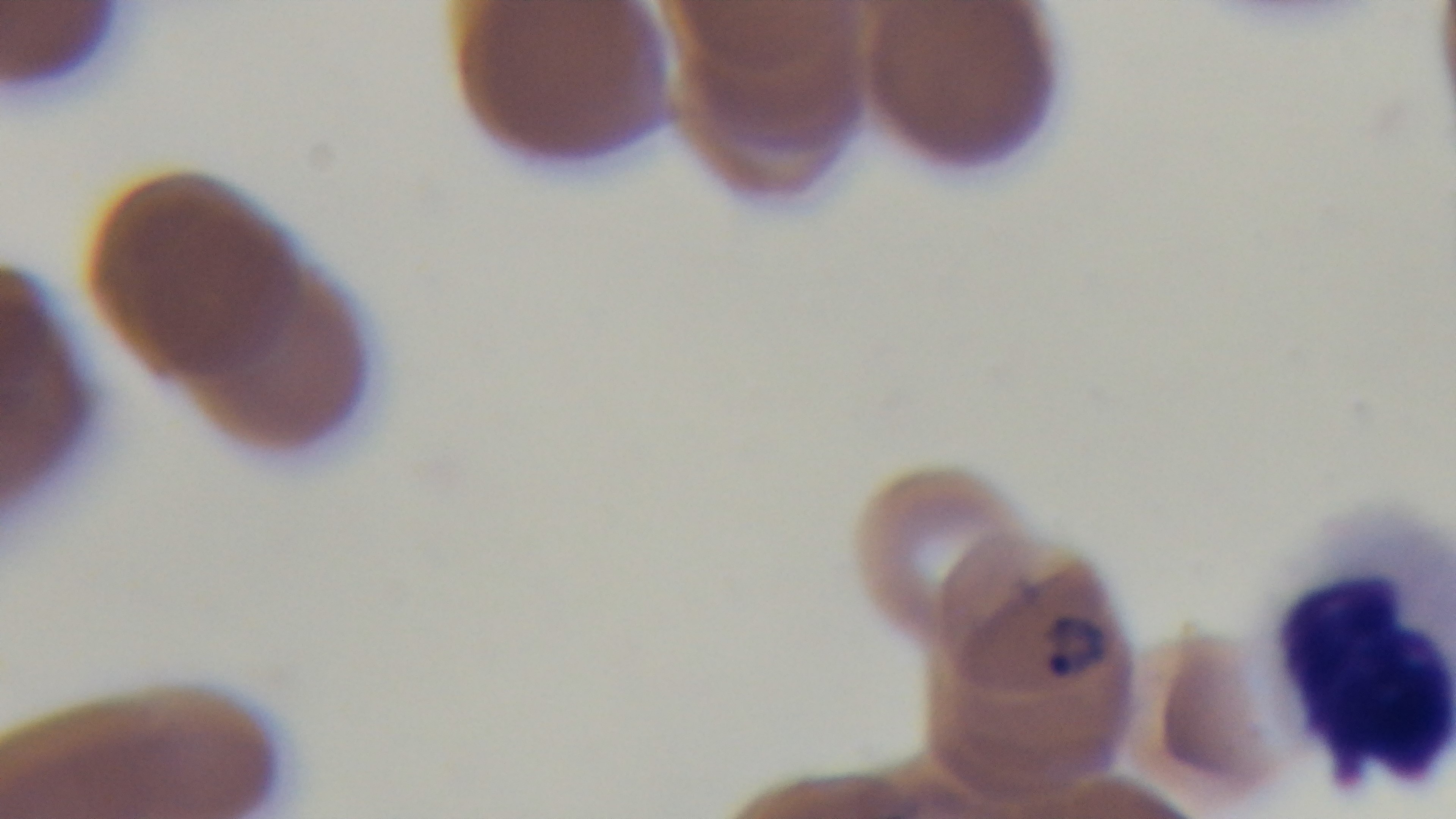

Summary:
  - Field of view: single
  - Capture: mounted 4K digital camera
  - Stain: Giemsa
  - Modality: light microscopy
  - Preparation: thin
  - Malaria status: infected
  - Objective: 100x oil immersion